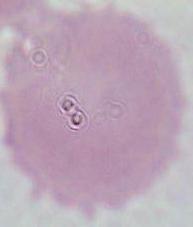 An erythrocyte is seen. Photomicrograph. Captured at 1000x magnification.